Classify the preparation.
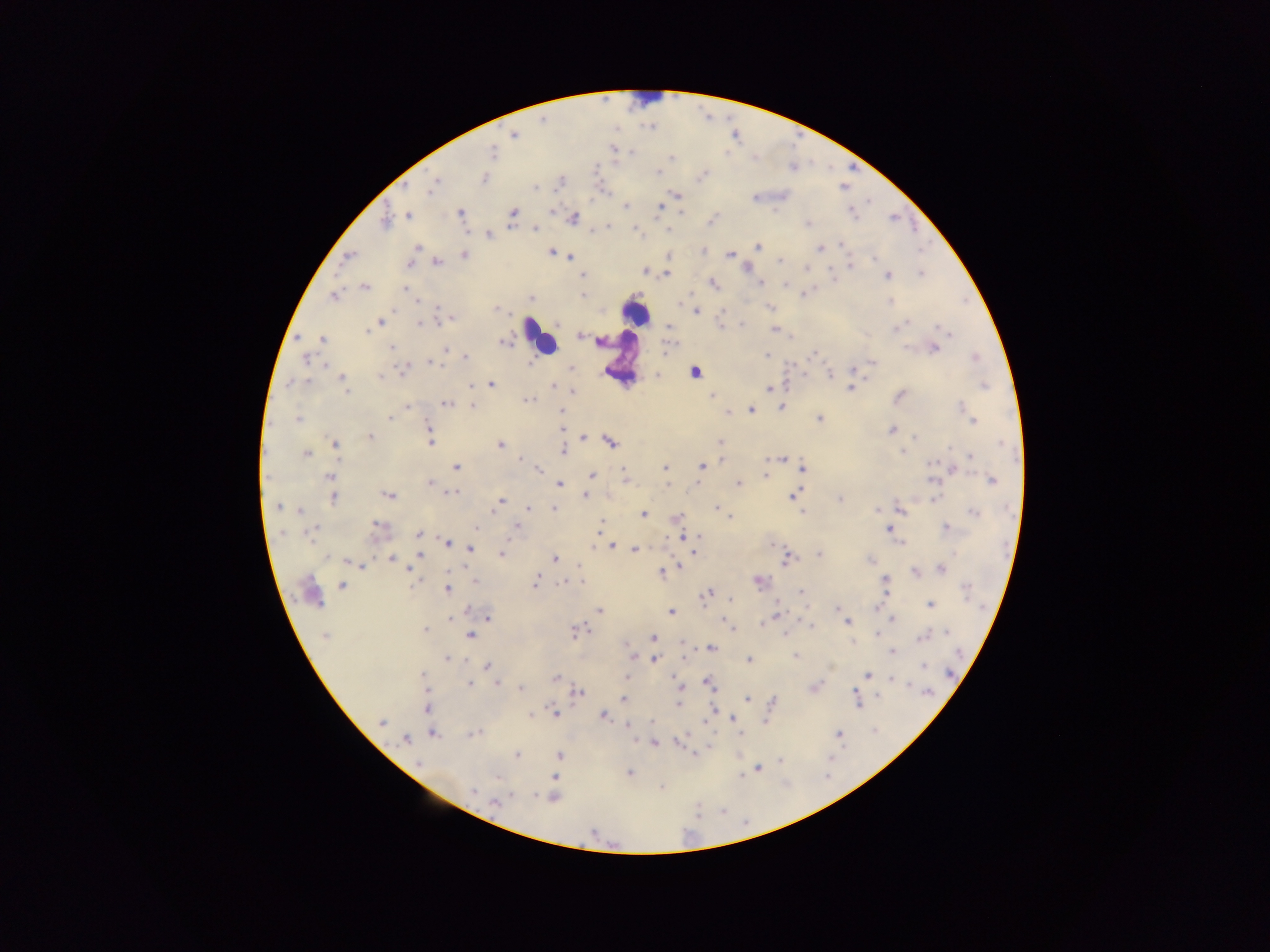
Thick blood smear.

{
  "country": "Ghana",
  "field_of_view": "single",
  "plasmodium_parasite_locations": "approximate centers as (x, y) in pixels: (514, 135), (493, 153), (631, 153), (672, 157), (657, 173), (703, 175), (485, 177), (433, 186), (534, 188), (678, 195), (755, 197), (626, 206), (660, 208), (551, 211), (681, 212), (461, 213), (512, 213), (852, 213), (408, 215), (573, 218), (385, 221), (808, 223), (535, 228), (488, 236), (840, 244), (417, 247), (757, 247), (820, 248), (702, 252), (551, 253), (464, 255), (570, 255), (730, 255), (348, 256), (669, 256), (780, 261), (437, 262), (409, 265), (850, 265), (806, 267), (645, 271), (648, 272), (666, 273), (921, 274), (888, 275), (583, 276), (712, 283), (759, 283), (784, 284), (364, 286), (405, 288), (806, 293), (581, 295), (333, 296), (531, 299), (417, 300), (890, 301), (438, 307), (770, 307), (497, 308), (696, 311), (448, 320), (381, 322), (420, 323), (557, 324), (669, 326), (720, 326), (742, 326), (898, 327), (774, 330), (367, 331), (945, 331), (579, 336), (322, 339), (504, 342), (602, 342), (937, 343), (667, 346), (391, 348), (934, 348), (446, 349), (767, 355), (812, 355), (467, 357), (976, 357), (306, 359), (430, 363), (872, 363), (531, 364), (326, 365), (405, 368), (571, 368), (852, 369), (695, 372), (829, 373), (342, 378), (381, 378), (305, 381), (291, 383), (491, 384), (552, 385), (985, 386), (471, 388), (769, 388), (851, 388), (348, 391), (573, 392), (711, 395), (899, 396), (529, 399), (446, 404), (407, 406), (471, 406), (782, 408), (963, 409), (750, 410), (561, 412), (727, 413), (390, 418), (820, 418), (297, 419), (972, 419), (429, 428), (892, 429), (562, 430), (370, 437), (583, 437), (915, 437), (431, 442), (611, 442), (720, 443), (335, 444), (500, 445), (563, 447), (564, 450), (903, 451), (306, 453), (971, 456), (520, 458), (781, 459), (932, 464), (702, 465), (456, 467), (666, 468), (803, 468), (539, 470), (764, 475), (591, 476), (623, 476), (330, 477), (991, 480), (430, 482), (738, 483), (560, 484), (450, 493), (389, 495), (791, 495), (585, 496), (333, 498), (934, 498), (840, 499), (500, 502), (278, 507), (528, 508), (553, 508), (902, 508), (717, 509), (877, 509), (299, 511), (974, 513), (644, 514), (730, 516), (677, 518), (376, 525), (517, 525), (601, 525), (476, 528), (947, 528), (311, 530), (889, 530), (283, 533), (309, 534), (418, 534), (683, 537), (699, 537), (447, 542), (900, 542), (773, 544), (612, 546), (470, 549), (635, 550), (694, 552), (502, 554), (819, 555), (327, 557), (391, 558), (555, 558), (869, 559), (787, 560), (361, 565), (680, 567), (410, 569), (941, 569), (661, 572), (915, 572), (759, 580), (475, 581), (581, 582), (886, 582), (535, 583), (565, 584), (342, 585), (446, 589), (966, 589), (801, 591), (706, 595), (730, 599), (930, 605), (837, 607), (467, 611), (600, 611), (671, 612), (776, 614), (488, 617), (450, 618), (892, 619), (725, 621), (846, 622), (762, 623), (731, 626), (810, 626), (425, 630), (577, 632), (946, 632), (784, 634), (325, 635), (471, 636), (653, 637), (921, 638), (853, 642), (711, 649), (892, 652), (632, 655), (795, 656), (447, 659), (655, 660), (749, 660), (488, 666), (924, 666), (867, 674), (422, 676), (627, 677), (555, 679), (895, 680), (677, 682), (709, 682), (496, 683), (470, 684), (680, 686), (815, 687), (520, 689), (425, 690), (577, 692), (927, 692), (855, 696), (623, 699), (747, 699), (774, 701), (858, 701), (678, 704), (426, 709), (713, 710), (530, 714), (556, 714), (604, 717), (734, 719), (382, 722), (652, 722), (629, 726), (474, 733), (433, 734), (839, 734), (741, 735), (410, 737), (405, 739), (654, 744), (694, 753), (517, 755), (559, 755), (781, 761), (419, 763), (758, 769), (630, 773), (741, 776), (499, 777), (554, 778), (660, 787), (473, 791), (512, 796), (535, 796), (553, 797), (495, 803)",
  "image_size": "1270×952 pixels",
  "capture": "mobile-phone photograph through a microscope",
  "leukocyte_locations": "approximate centers as (x, y) in pixels: (645, 93), (635, 313), (540, 337)"
}